Describe the morphology of the erythrocytes.
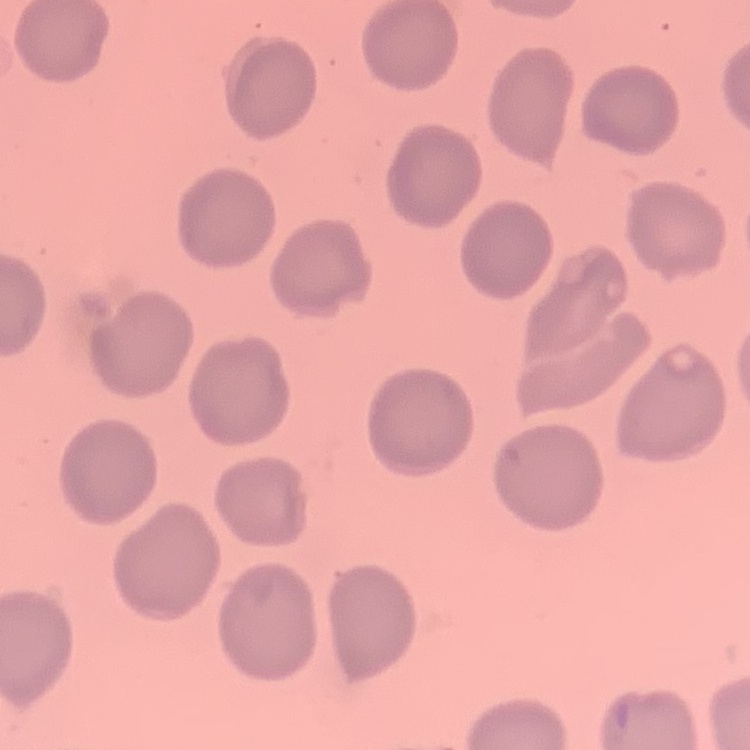
They show no rouleaux formation.

image_type: square crop of a larger photomicrograph
stain: Field's or Giemsa
preparation: thin peripheral smear